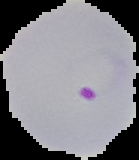 Segmented cell region on a black background. Image is 139×160 pixels. From a thin blood smear. Malaria status: parasitized.